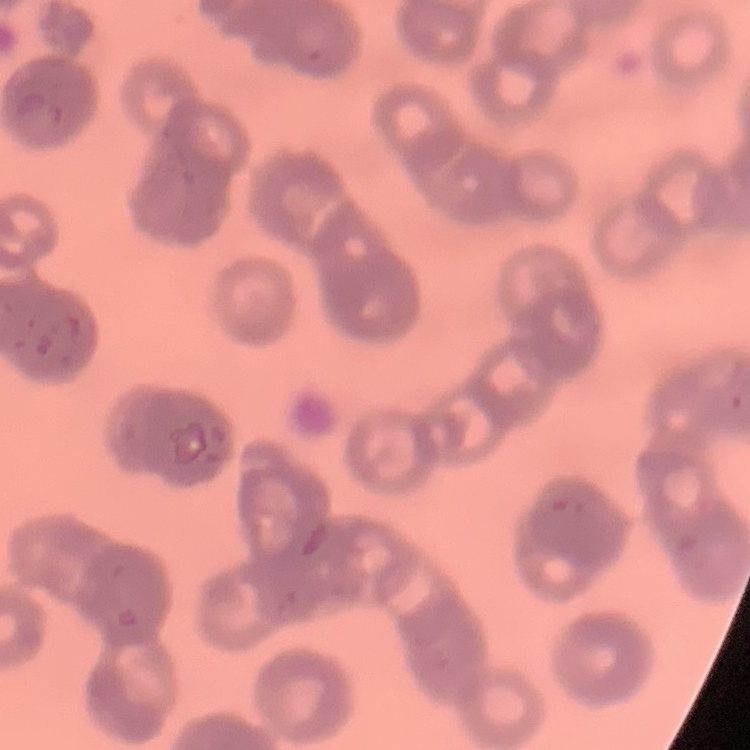

erythrocyte morphology = rouleaux formation
image type = square crop of a larger photomicrograph
stain = Field's or Giemsa
preparation = thin blood smear